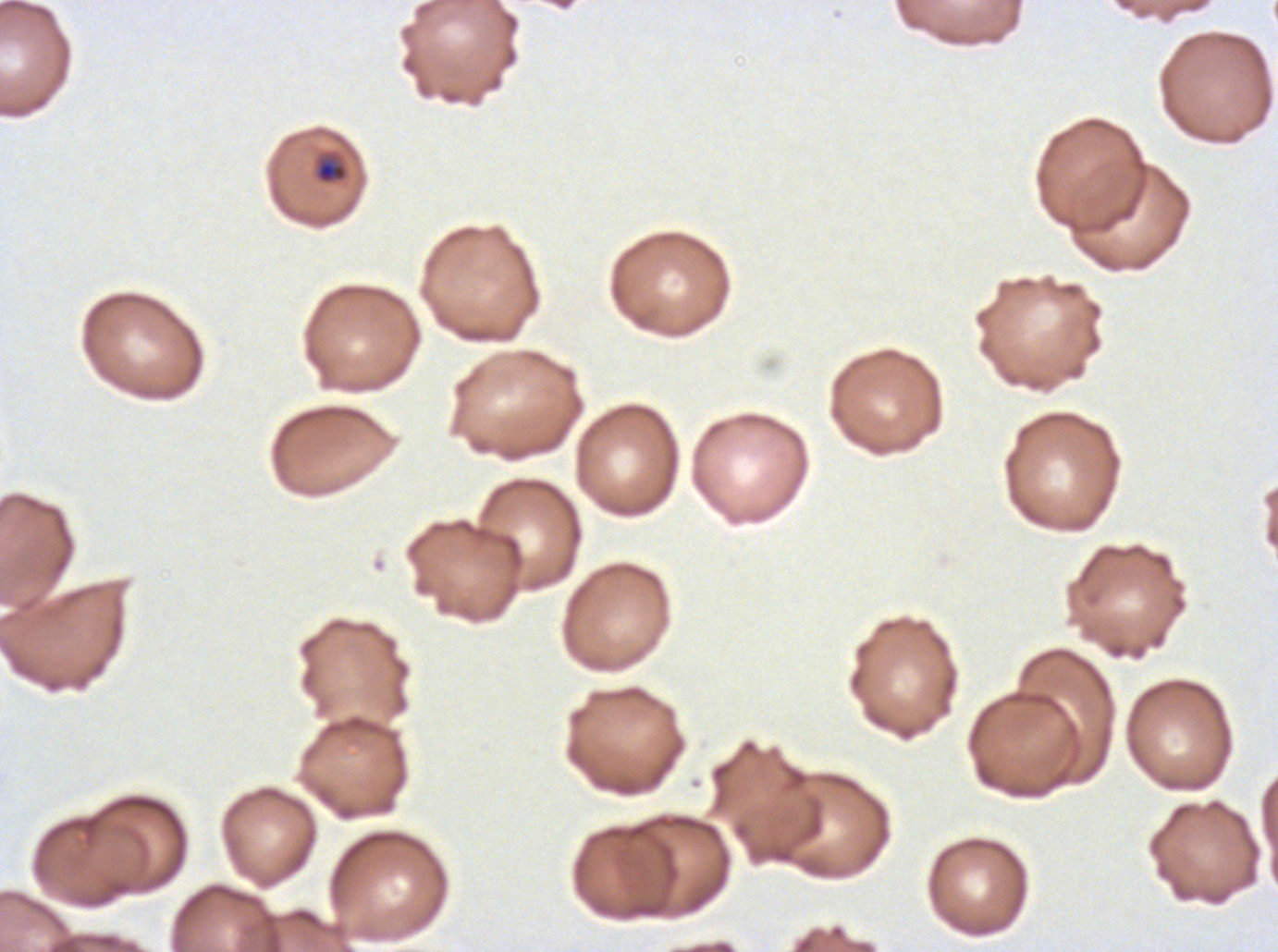

notation = approximate bounding boxes as {x1, y1, x2, y2} in pixels
late-ring/early-trophozoite locations = {313, 152, 349, 185}
preparation = thin blood film
specimen = ex-vivo Plasmodium falciparum culture from a patient in The Gambia, grown for 24 to 48 hours
stain = Giemsa
field of view = one sub-image of a larger composite
image size = 1278×952 pixels